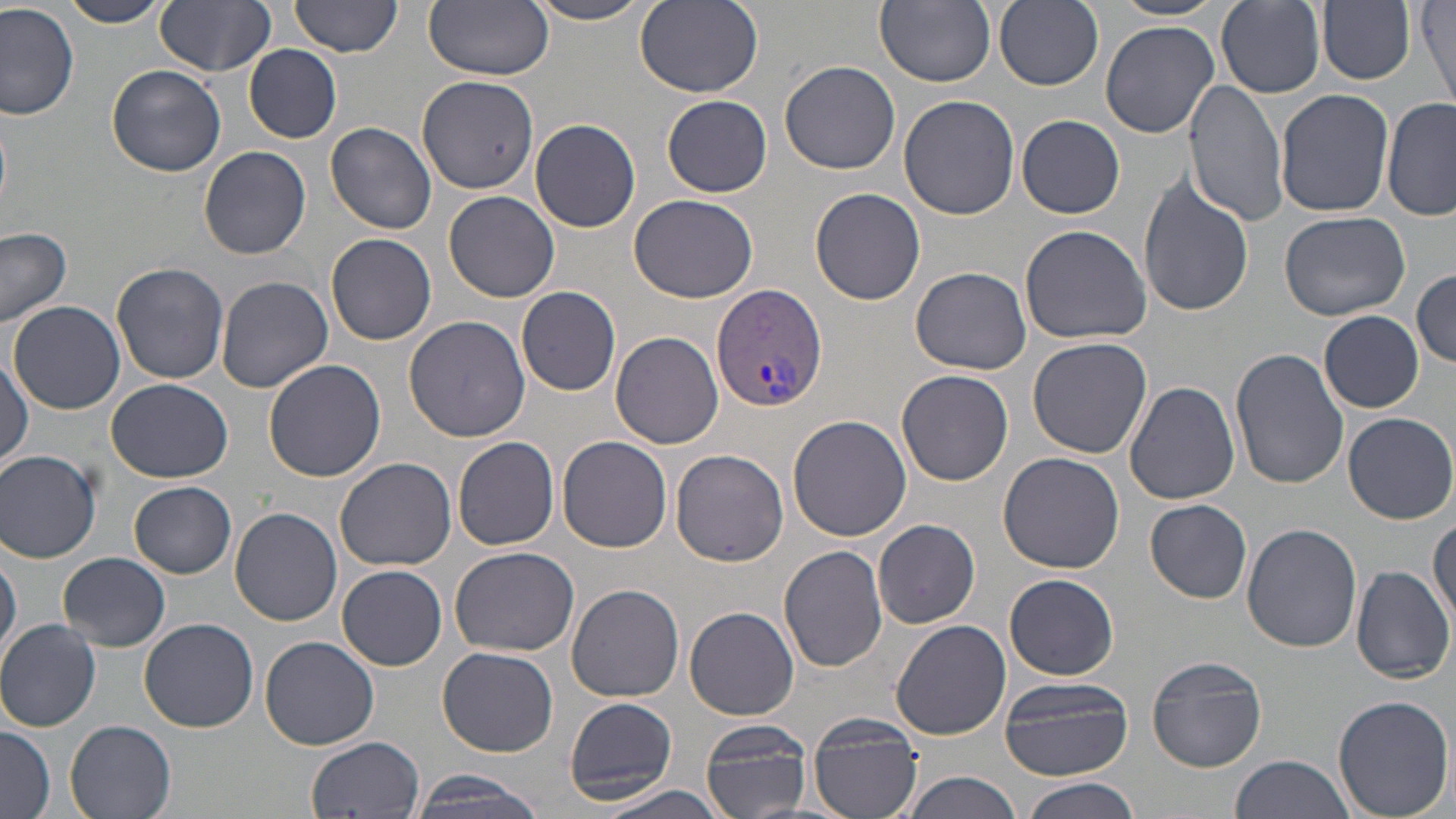

Summary:
  - Coordinate format: approximate bounding boxes as named x1/y1/x2/y2 corners in pixels
  - Uninfected red blood cell locations: (x1=57, y1=0, x2=173, y2=28), (x1=291, y1=0, x2=402, y2=57), (x1=876, y1=0, x2=996, y2=88), (x1=994, y1=0, x2=1103, y2=89), (x1=1110, y1=0, x2=1229, y2=22), (x1=154, y1=1, x2=276, y2=76), (x1=425, y1=1, x2=555, y2=79), (x1=522, y1=1, x2=660, y2=25), (x1=633, y1=1, x2=763, y2=98), (x1=1318, y1=1, x2=1415, y2=86), (x1=1214, y1=2, x2=1326, y2=100), (x1=1418, y1=2, x2=1454, y2=112), (x1=0, y1=3, x2=79, y2=120), (x1=1100, y1=21, x2=1218, y2=139), (x1=244, y1=44, x2=342, y2=143), (x1=779, y1=61, x2=900, y2=176), (x1=108, y1=66, x2=226, y2=177), (x1=417, y1=73, x2=541, y2=195), (x1=1187, y1=79, x2=1290, y2=225), (x1=1275, y1=89, x2=1394, y2=218), (x1=662, y1=95, x2=772, y2=197), (x1=899, y1=95, x2=1020, y2=221), (x1=1382, y1=97, x2=1455, y2=223), (x1=1017, y1=114, x2=1124, y2=218), (x1=530, y1=119, x2=641, y2=233), (x1=324, y1=122, x2=438, y2=235), (x1=198, y1=146, x2=313, y2=260), (x1=1137, y1=172, x2=1253, y2=319), (x1=812, y1=187, x2=925, y2=306), (x1=444, y1=191, x2=560, y2=303), (x1=629, y1=194, x2=759, y2=304), (x1=1277, y1=209, x2=1412, y2=321), (x1=1020, y1=225, x2=1152, y2=346), (x1=0, y1=228, x2=73, y2=330), (x1=326, y1=233, x2=438, y2=346), (x1=112, y1=263, x2=228, y2=385), (x1=912, y1=267, x2=1034, y2=376), (x1=1412, y1=267, x2=1456, y2=369), (x1=216, y1=276, x2=334, y2=391), (x1=517, y1=286, x2=621, y2=394), (x1=11, y1=301, x2=125, y2=415), (x1=1318, y1=310, x2=1424, y2=412), (x1=403, y1=316, x2=531, y2=443), (x1=612, y1=331, x2=722, y2=449), (x1=1026, y1=337, x2=1152, y2=460), (x1=1229, y1=347, x2=1346, y2=488), (x1=0, y1=357, x2=31, y2=472), (x1=263, y1=358, x2=385, y2=482), (x1=898, y1=370, x2=1014, y2=487), (x1=106, y1=379, x2=236, y2=483), (x1=1124, y1=381, x2=1240, y2=504), (x1=1344, y1=412, x2=1456, y2=524), (x1=786, y1=413, x2=912, y2=543), (x1=453, y1=436, x2=560, y2=550), (x1=558, y1=436, x2=673, y2=552), (x1=670, y1=448, x2=790, y2=567), (x1=0, y1=449, x2=102, y2=564), (x1=997, y1=451, x2=1125, y2=573), (x1=334, y1=457, x2=457, y2=572), (x1=129, y1=482, x2=237, y2=578), (x1=1145, y1=499, x2=1252, y2=603), (x1=230, y1=507, x2=342, y2=625), (x1=1428, y1=515, x2=1455, y2=629), (x1=873, y1=519, x2=980, y2=629), (x1=1242, y1=521, x2=1363, y2=651), (x1=450, y1=545, x2=580, y2=657), (x1=779, y1=545, x2=889, y2=673), (x1=1, y1=549, x2=21, y2=662), (x1=59, y1=553, x2=171, y2=650), (x1=338, y1=565, x2=447, y2=670), (x1=1349, y1=565, x2=1456, y2=682), (x1=1003, y1=573, x2=1121, y2=681), (x1=566, y1=582, x2=684, y2=702), (x1=684, y1=607, x2=799, y2=720), (x1=138, y1=617, x2=259, y2=732), (x1=890, y1=618, x2=1011, y2=741), (x1=0, y1=619, x2=101, y2=732), (x1=261, y1=636, x2=380, y2=749), (x1=438, y1=648, x2=560, y2=756), (x1=1147, y1=655, x2=1267, y2=772), (x1=1000, y1=675, x2=1135, y2=781), (x1=563, y1=696, x2=678, y2=803), (x1=1332, y1=696, x2=1454, y2=819), (x1=807, y1=712, x2=924, y2=819), (x1=700, y1=718, x2=814, y2=819), (x1=65, y1=719, x2=178, y2=819), (x1=0, y1=724, x2=53, y2=819), (x1=306, y1=736, x2=425, y2=819), (x1=1229, y1=755, x2=1353, y2=819), (x1=898, y1=770, x2=1022, y2=819), (x1=410, y1=771, x2=551, y2=818), (x1=1020, y1=778, x2=1143, y2=819), (x1=591, y1=783, x2=733, y2=819)
  - Plasmodium vivax-infected red blood cell locations: (x1=713, y1=283, x2=827, y2=411)
  - Slide-level diagnosis: Plasmodium vivax
  - Magnification: 1000x
  - Modality: light microscopy
  - Stain: May-Grünwald-Giemsa
  - Preparation: thin blood film
  - Image size: 1456×819 pixels
  - Field of view: one of a larger specimen